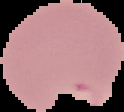
Image is 124×112 pixels. Segmented cell region on a black background. Malaria status: parasitized. From a thin blood smear.